Identify the cell.
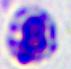

A leukocyte.

Summary:
  - Magnification: 400x
  - Modality: micrograph